Point out each malaria parasite.
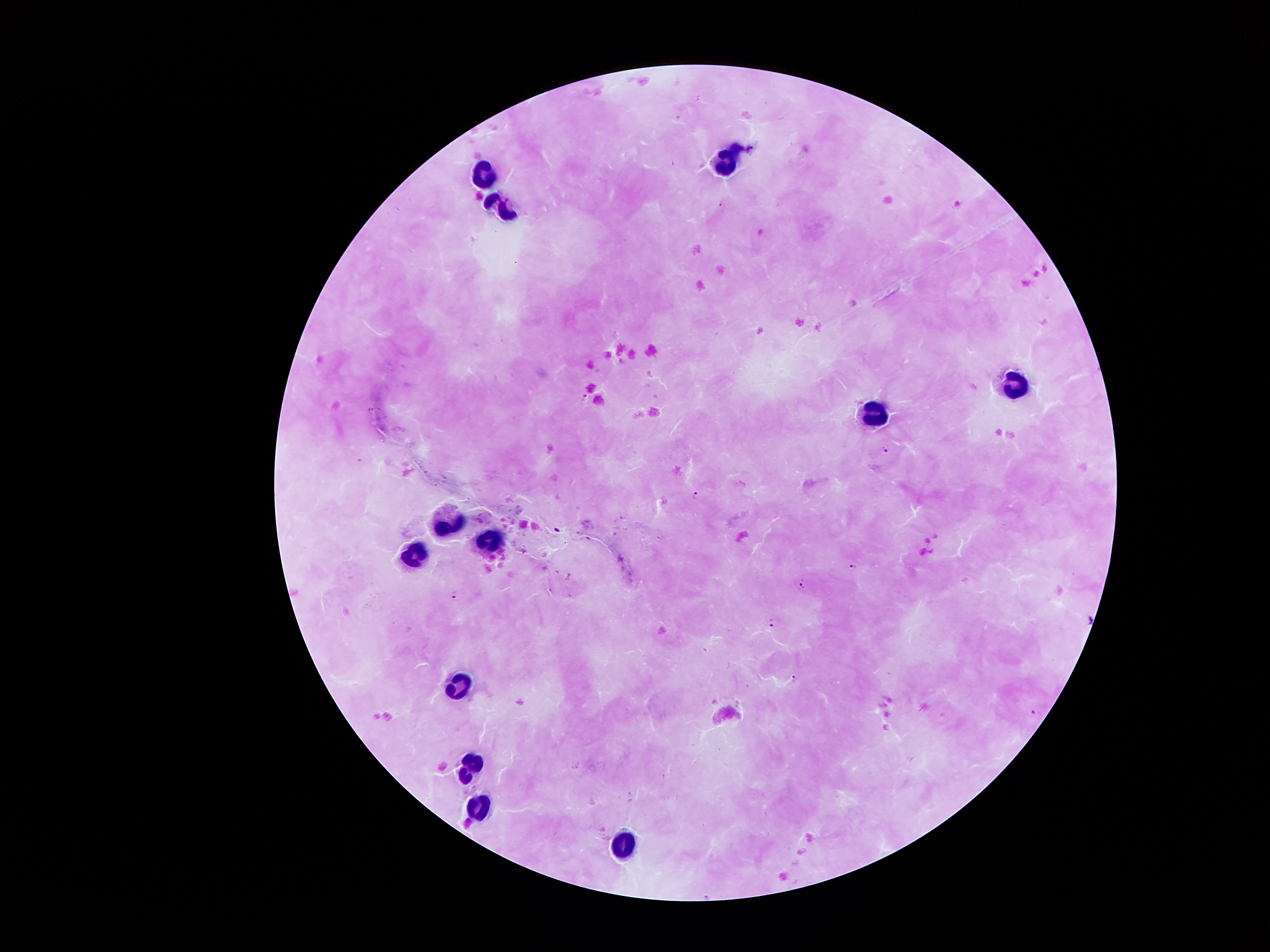

Approximate centers as [x, y] in pixels.
Malaria parasites: [721, 203], [583, 398], [886, 448], [696, 494], [853, 568], [802, 585], [455, 594], [773, 622], [795, 678], [1035, 713].

Leukocyte locations: [727, 155], [486, 172], [500, 207], [1016, 380], [875, 411], [449, 519], [493, 542], [416, 556], [461, 685], [473, 763], [480, 801], [626, 842]. Single field of view. Giemsa-stained preparation. 100x magnification. Photographed through the microscope eyepiece with a smartphone camera. Image is 1270×952 pixels. Patient malaria status: infected with Plasmodium falciparum. Thick blood film.